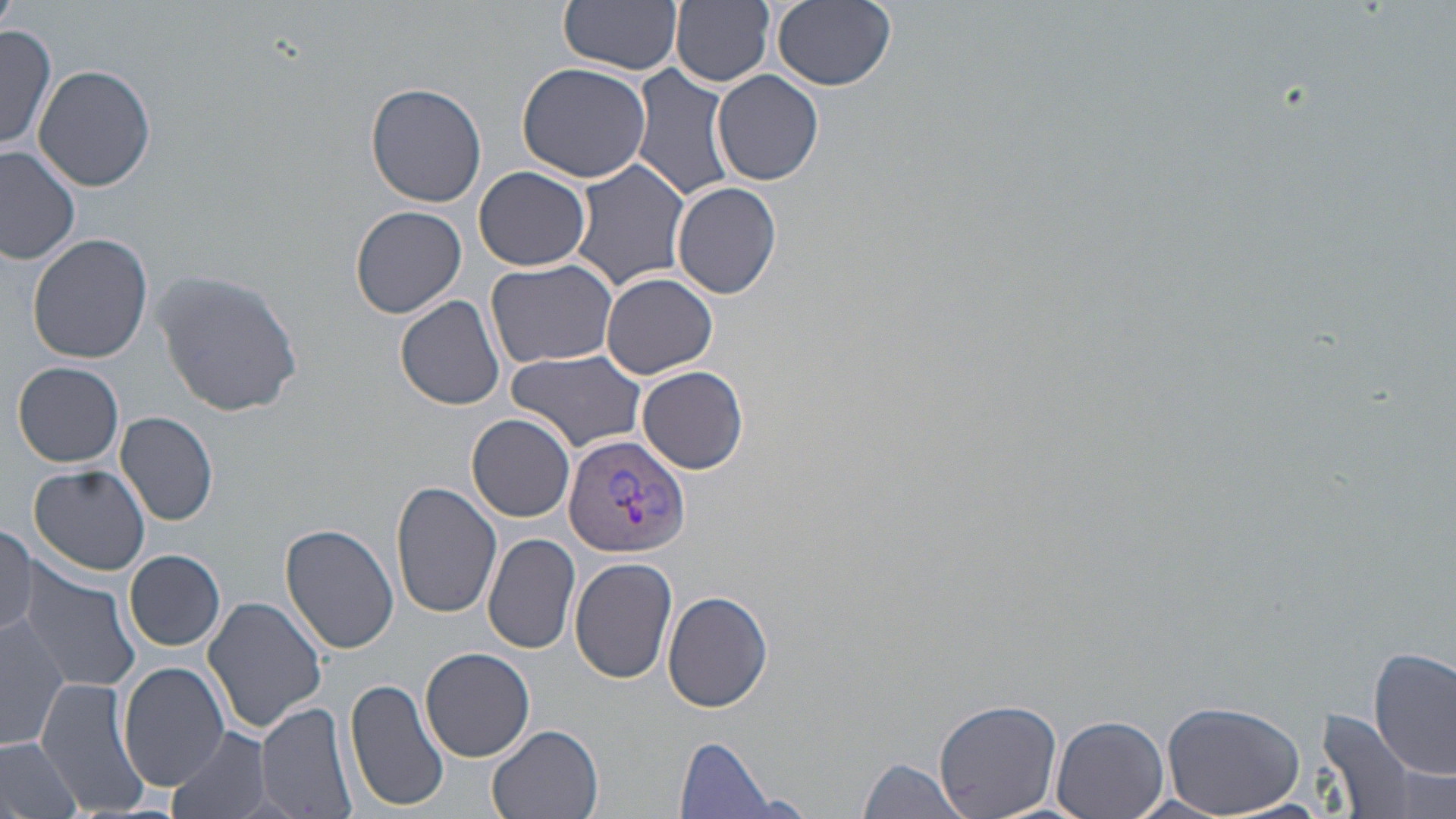 Approximate bounding boxes as named x1/y1/x2/y2 corners in pixels. Uninfected red blood cell locations: (x1=0, y1=0, x2=19, y2=33), (x1=560, y1=0, x2=683, y2=75), (x1=771, y1=0, x2=897, y2=91), (x1=671, y1=1, x2=775, y2=87), (x1=0, y1=24, x2=55, y2=155), (x1=517, y1=62, x2=653, y2=183), (x1=33, y1=63, x2=159, y2=191), (x1=631, y1=64, x2=734, y2=207), (x1=713, y1=70, x2=824, y2=186), (x1=365, y1=81, x2=488, y2=208), (x1=0, y1=147, x2=80, y2=265), (x1=569, y1=157, x2=692, y2=291), (x1=474, y1=166, x2=591, y2=271), (x1=671, y1=180, x2=782, y2=300), (x1=351, y1=204, x2=468, y2=318), (x1=27, y1=234, x2=153, y2=363), (x1=486, y1=258, x2=618, y2=369), (x1=151, y1=268, x2=304, y2=418), (x1=602, y1=273, x2=718, y2=379), (x1=395, y1=293, x2=506, y2=410), (x1=505, y1=350, x2=646, y2=453), (x1=13, y1=361, x2=126, y2=468), (x1=637, y1=366, x2=750, y2=474), (x1=116, y1=410, x2=220, y2=526), (x1=468, y1=414, x2=575, y2=521), (x1=29, y1=465, x2=150, y2=575), (x1=391, y1=480, x2=502, y2=620), (x1=0, y1=523, x2=38, y2=637), (x1=280, y1=523, x2=400, y2=653), (x1=483, y1=533, x2=581, y2=654), (x1=125, y1=550, x2=226, y2=651), (x1=569, y1=556, x2=679, y2=683), (x1=17, y1=564, x2=147, y2=697), (x1=663, y1=590, x2=773, y2=712), (x1=202, y1=595, x2=329, y2=732), (x1=2, y1=613, x2=69, y2=753), (x1=421, y1=647, x2=535, y2=762), (x1=1370, y1=648, x2=1454, y2=778), (x1=117, y1=662, x2=229, y2=791), (x1=345, y1=677, x2=447, y2=812), (x1=34, y1=679, x2=150, y2=819), (x1=935, y1=698, x2=1061, y2=818), (x1=1160, y1=700, x2=1306, y2=817), (x1=256, y1=701, x2=359, y2=819), (x1=1318, y1=711, x2=1418, y2=815), (x1=1051, y1=714, x2=1170, y2=819), (x1=166, y1=725, x2=275, y2=819), (x1=489, y1=726, x2=601, y2=819), (x1=0, y1=734, x2=82, y2=819), (x1=677, y1=737, x2=778, y2=817), (x1=858, y1=757, x2=968, y2=818). Plasmodium vivax-infected red blood cell locations: (x1=563, y1=434, x2=692, y2=558). Slide-level diagnosis: Plasmodium vivax. Optical microscopy. Captured at 1000x magnification. Thin blood smear. Image is 1456×819 pixels. May-Grünwald-Giemsa stain. Single field of view.